Locate every Plasmodium parasite.
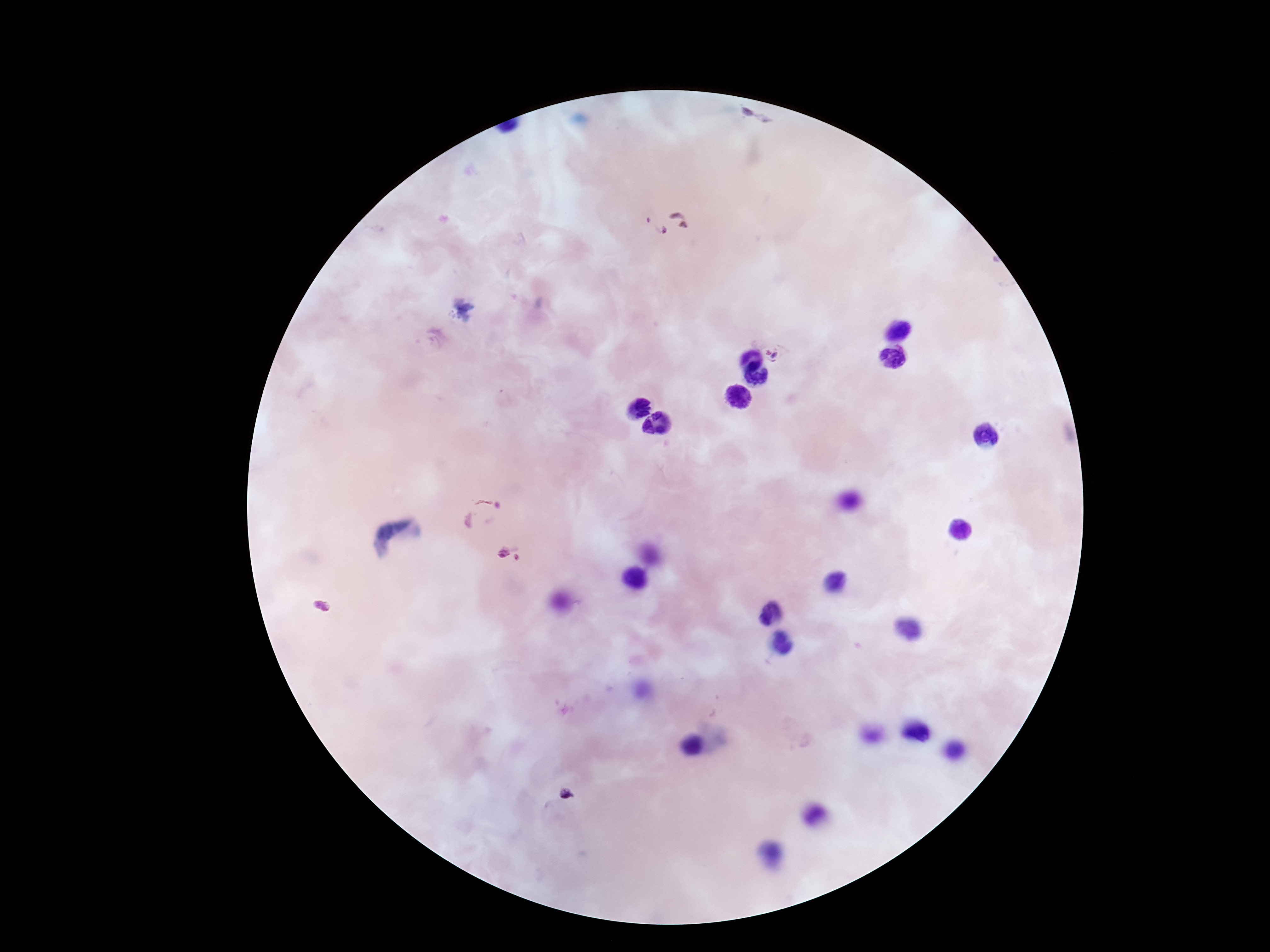

Approximate object centers, in pixels from the top-left corner.
Plasmodium parasites: (x=752, y=118), (x=665, y=224), (x=774, y=354), (x=480, y=515), (x=502, y=553), (x=518, y=556), (x=322, y=607).

Summary:
  - Capture: smartphone camera through the microscope eyepiece
  - Patient malaria status: infected
  - Image size: 1270×952 pixels
  - Field of view: one from this slide
  - Preparation: thick peripheral-blood smear
  - Stain: Giemsa
  - Magnification: 100x